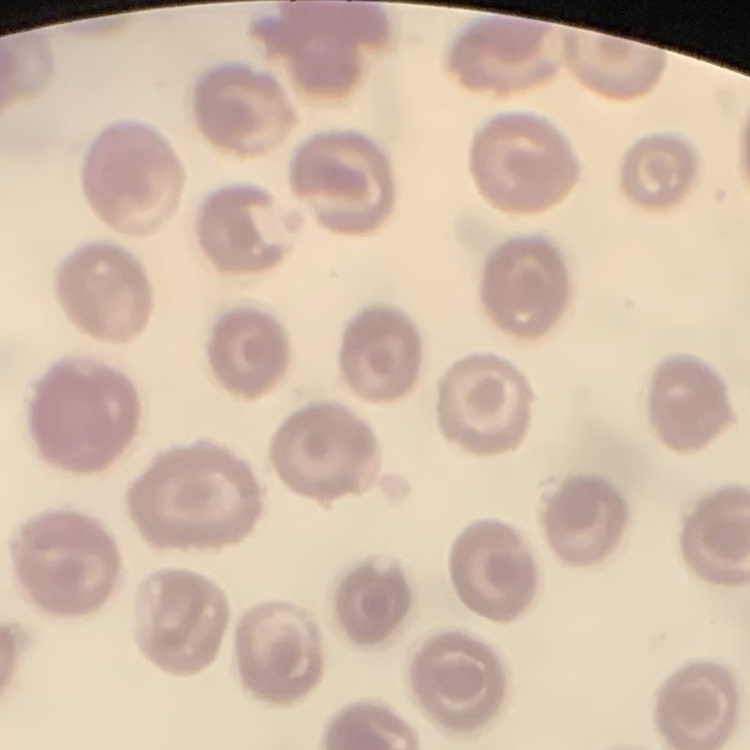

Summary:
  - Red blood cell morphology: no rouleaux formation
  - Image type: square crop of a larger photomicrograph
  - Stain: Field's or Giemsa
  - Preparation: thin blood smear